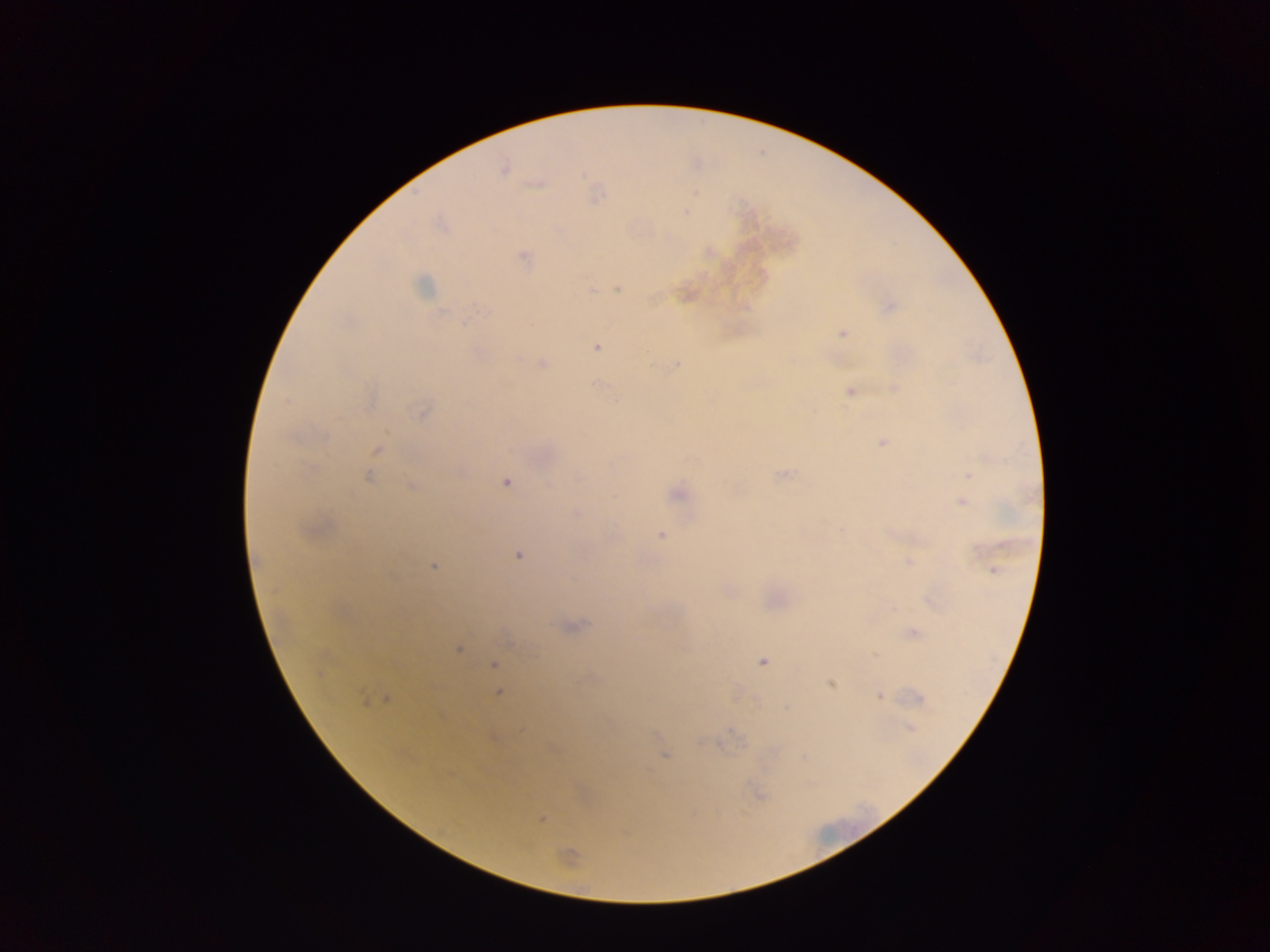
{
  "preparation": "thick blood film",
  "image_size": "1270×952 pixels",
  "plasmodium_parasite_locations": "approximate centers as {x, y} in pixels: {503, 168}, {537, 183}, {442, 224}, {709, 251}, {523, 258}, {424, 285}, {591, 289}, {618, 289}, {685, 293}, {889, 306}, {843, 333}, {596, 346}, {542, 363}, {676, 363}, {597, 386}, {896, 389}, {851, 391}, {423, 410}, {882, 441}, {376, 449}, {782, 474}, {969, 474}, {367, 476}, {505, 481}, {411, 486}, {736, 488}, {677, 493}, {963, 502}, {577, 512}, {313, 529}, {661, 535}, {518, 555}, {910, 562}, {433, 565}, {995, 570}, {727, 591}, {932, 599}, {570, 627}, {913, 631}, {510, 641}, {458, 648}, {762, 660}, {495, 665}, {830, 684}, {498, 692}, {737, 693}, {879, 695}, {373, 698}, {915, 698}, {787, 708}, {911, 727}, {664, 755}, {758, 794}, {541, 818}, {567, 857}",
  "capture": "mobile-phone photograph through a microscope",
  "country": "Ghana",
  "field_of_view": "single"
}